Classify this cell by malaria status.
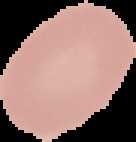
Uninfected.

{
  "image_size": "136×142 pixels",
  "image_type": "segmented cell region with the area outside set to black",
  "preparation": "thin blood film"
}